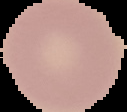
Image is 127×112 pixels. Segmented cell region on a black background. From a thin blood smear. Malaria status: uninfected.